Classify this cell by malaria status.
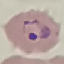
Parasitized.

Summary:
  - Image type: automatically extracted cell patch, resized to 64 × 64 pixels
  - Preparation: thin smear
  - Capture: smartphone through the microscope eyepiece
  - Stain: Giemsa